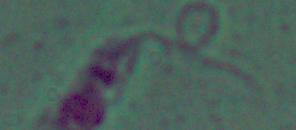 Photomicrograph. Captured at 1000x magnification. A Leishmania parasite is shown.